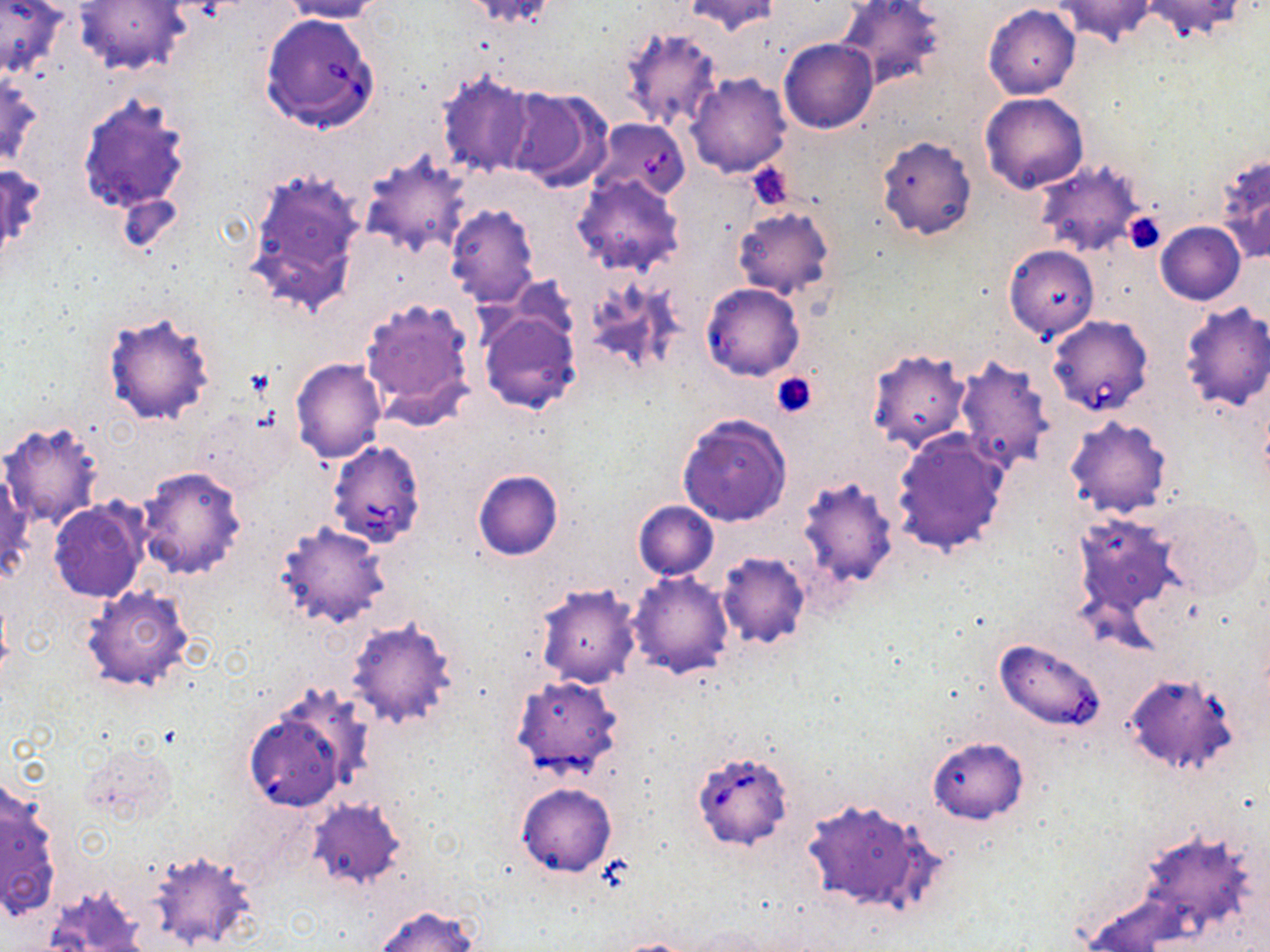

Approximate bounding boxes as [x1, y1, x2, y2] in pixels. Babesia divergens-infected red blood cell locations: [260, 12, 380, 132], [589, 120, 691, 203], [1047, 315, 1154, 415], [327, 440, 427, 549], [510, 676, 623, 780], [691, 751, 792, 850]. Platelet locations: [747, 164, 794, 211], [1125, 214, 1166, 255], [771, 372, 818, 418]. Uninfected red blood cell locations: [0, 0, 67, 78], [278, 0, 386, 22], [684, 0, 781, 37], [837, 0, 947, 92], [1052, 0, 1156, 45], [1140, 0, 1249, 40], [77, 1, 188, 75], [461, 1, 564, 28], [982, 4, 1081, 100], [621, 24, 725, 133], [779, 39, 877, 134], [436, 69, 537, 181], [686, 73, 792, 177], [1, 74, 43, 168], [503, 86, 611, 192], [77, 92, 192, 214], [979, 92, 1089, 193], [877, 135, 977, 240], [359, 149, 471, 259], [1213, 149, 1270, 264], [0, 160, 46, 259], [1034, 161, 1145, 257], [244, 168, 366, 319], [572, 173, 685, 278], [445, 204, 539, 307], [733, 208, 835, 299], [1155, 222, 1245, 306], [1004, 244, 1099, 340], [358, 295, 478, 426], [1177, 303, 1270, 412], [477, 305, 582, 414], [101, 310, 217, 427], [865, 348, 971, 454], [953, 357, 1056, 472], [290, 358, 387, 463], [193, 406, 296, 494], [677, 412, 792, 526], [1063, 416, 1172, 519], [1, 421, 104, 530], [891, 429, 1012, 558], [1, 465, 31, 580], [135, 465, 248, 580], [472, 468, 564, 560], [796, 475, 898, 589], [47, 486, 241, 592], [1153, 497, 1263, 599], [48, 498, 149, 603], [633, 500, 718, 581], [1071, 512, 1184, 628], [272, 520, 391, 629], [716, 551, 811, 650], [627, 572, 733, 679], [535, 582, 641, 688], [81, 584, 196, 693], [346, 617, 459, 730], [991, 640, 1107, 736], [1122, 673, 1241, 778], [244, 706, 356, 811], [927, 736, 1028, 824], [79, 743, 177, 825], [1, 780, 61, 919], [516, 783, 617, 876], [307, 798, 406, 890], [802, 798, 933, 913], [147, 851, 256, 950], [44, 884, 152, 952], [373, 905, 480, 952], [614, 938, 703, 952]. Slide-level diagnosis: Babesia divergens. Single field of view. May-Grünwald-Giemsa stain. Image is 1270×952 pixels. 1000x magnification. Thin blood film. Optical microscopy.